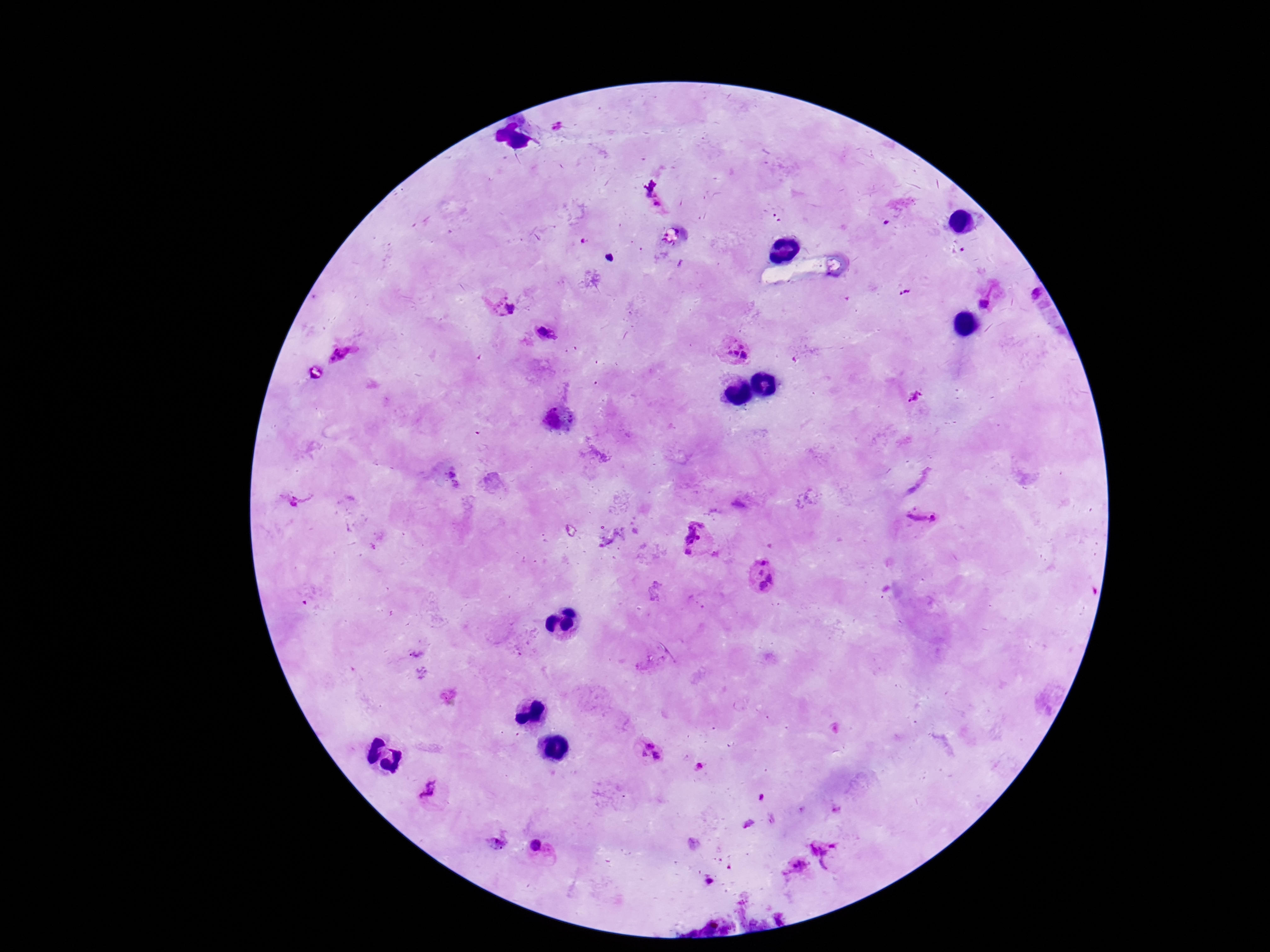

patient_malaria_status: infected
field_of_view: single
preparation: thick peripheral-blood smear
plasmodium_parasite_locations: 'approximate centers as (x, y) in pixels: (558, 126), (658, 204), (993, 293), (1036, 295), (501, 305), (545, 332), (735, 353), (341, 360), (915, 399), (920, 520), (699, 540), (762, 575), (646, 750), (431, 793), (538, 847), (823, 851), (795, 869)'
stain: Giemsa
capture: smartphone camera through the microscope eyepiece
image_size: 1270×952 pixels
magnification: 100x